Assess the morphology of the erythrocytes.
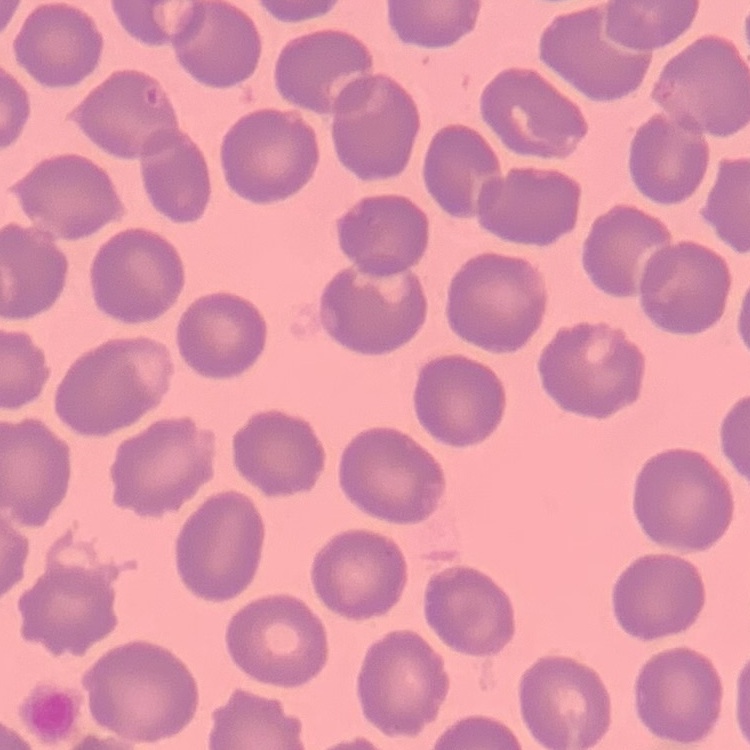
They show no rouleaux formation.

Summary:
  - Stain: Field's or Giemsa
  - Preparation: thin blood smear
  - Image type: square crop of a larger photomicrograph